Locate every uninfected red blood cell.
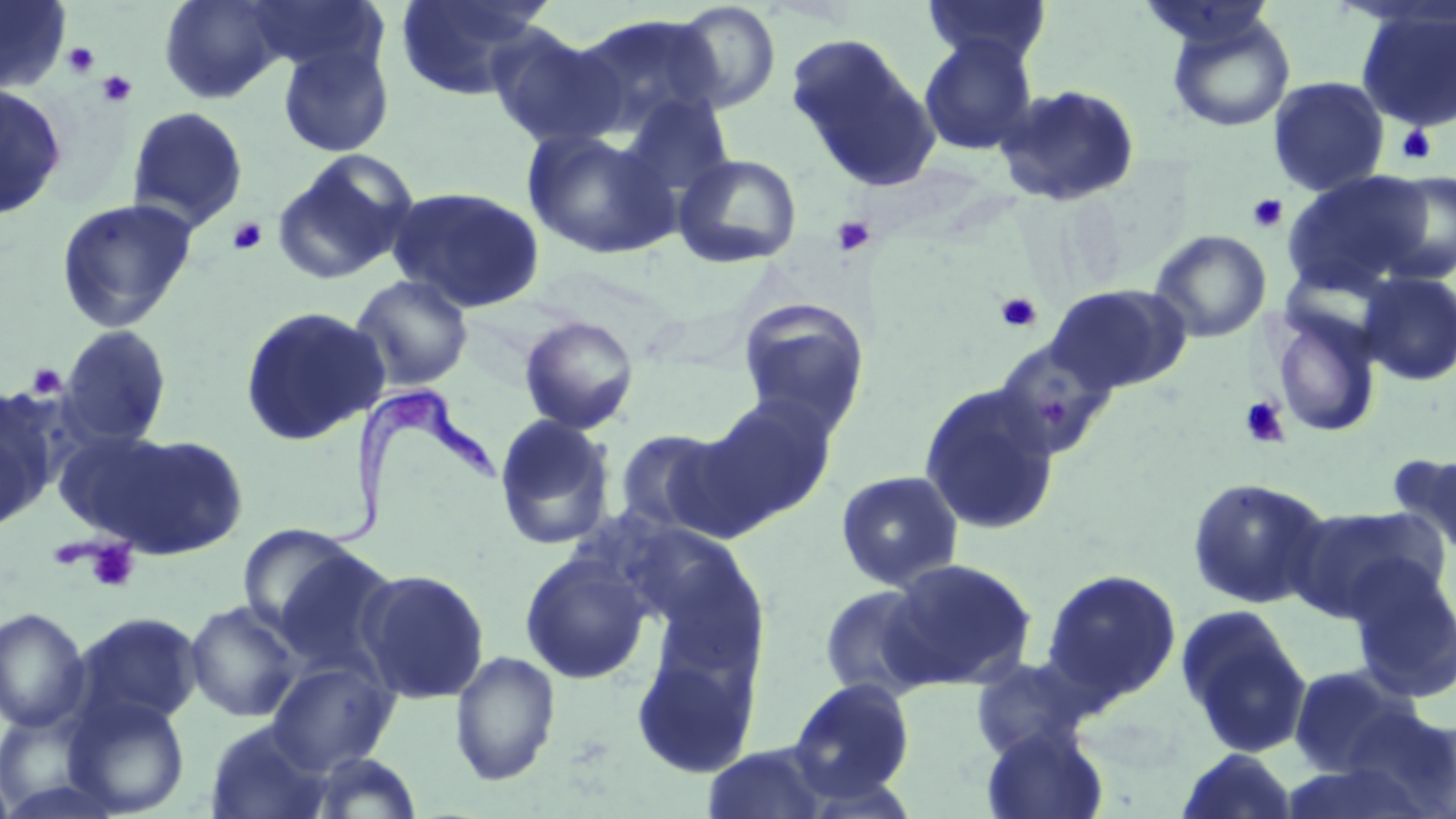
Approximate bounding boxes as (x1, y1, x2, y2) in pixels.
Uninfected red blood cells (subset): (158, 0, 288, 104), (395, 0, 548, 101), (921, 0, 1053, 67), (242, 1, 390, 79), (671, 1, 782, 113), (1355, 6, 1456, 133), (569, 13, 728, 139), (1165, 13, 1296, 133), (486, 26, 625, 150), (785, 33, 939, 191), (918, 36, 1038, 156), (277, 42, 395, 158), (1267, 76, 1389, 197), (0, 82, 68, 220), (993, 83, 1142, 208), (617, 92, 737, 210), (126, 106, 248, 231), (522, 129, 679, 260), (270, 150, 420, 287), (672, 152, 803, 269), (1282, 170, 1438, 296), (1375, 171, 1456, 285), (387, 186, 547, 313), (55, 198, 198, 333), (1149, 229, 1272, 343), (1357, 271, 1456, 386), (350, 274, 474, 391), (1044, 283, 1192, 395), (736, 296, 871, 435), (239, 305, 390, 446), (1268, 307, 1382, 438), (519, 315, 640, 435), (58, 325, 172, 448), (993, 337, 1119, 458), (917, 382, 1062, 536), (0, 388, 62, 521), (695, 393, 840, 531), (494, 415, 617, 551), (611, 427, 733, 537), (51, 429, 177, 540), (93, 433, 250, 560), (1396, 451, 1456, 557), (834, 470, 964, 592), (1186, 477, 1331, 609), (1287, 503, 1452, 623), (237, 523, 365, 637), (268, 545, 403, 680), (519, 550, 652, 684), (882, 557, 1039, 691), (1346, 560, 1456, 703), (356, 568, 490, 704), (1041, 568, 1182, 708), (818, 584, 941, 702), (185, 600, 303, 722), (1175, 606, 1313, 758), (0, 607, 90, 733), (73, 612, 204, 730), (630, 645, 759, 779), (449, 649, 561, 787), (969, 656, 1092, 763), (266, 659, 399, 774), (1287, 664, 1420, 778), (785, 676, 916, 804), (64, 695, 190, 817), (1340, 705, 1456, 815), (0, 708, 113, 817), (204, 721, 335, 819), (980, 725, 1111, 819), (701, 741, 838, 819), (1176, 748, 1299, 819), (302, 750, 424, 818).

Summary:
  - Trypanosoma brucei locations: (306, 385, 501, 558)
  - Platelet locations (subset): (63, 42, 100, 77), (97, 71, 137, 108), (1395, 124, 1437, 166), (1247, 193, 1289, 233), (831, 216, 876, 258), (226, 217, 268, 256), (994, 292, 1044, 333), (26, 363, 67, 400), (1238, 396, 1291, 449), (84, 540, 140, 592)
  - Slide-level diagnosis: Trypanosoma brucei
  - Field of view: single
  - Image size: 1456×819 pixels
  - Modality: optical microscopy
  - Preparation: thin blood film
  - Magnification: 1000x
  - Stain: May-Grünwald-Giemsa